Name the parasite shown.
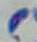
This is Toxoplasma gondii.

1000x magnification. Photomicrograph.